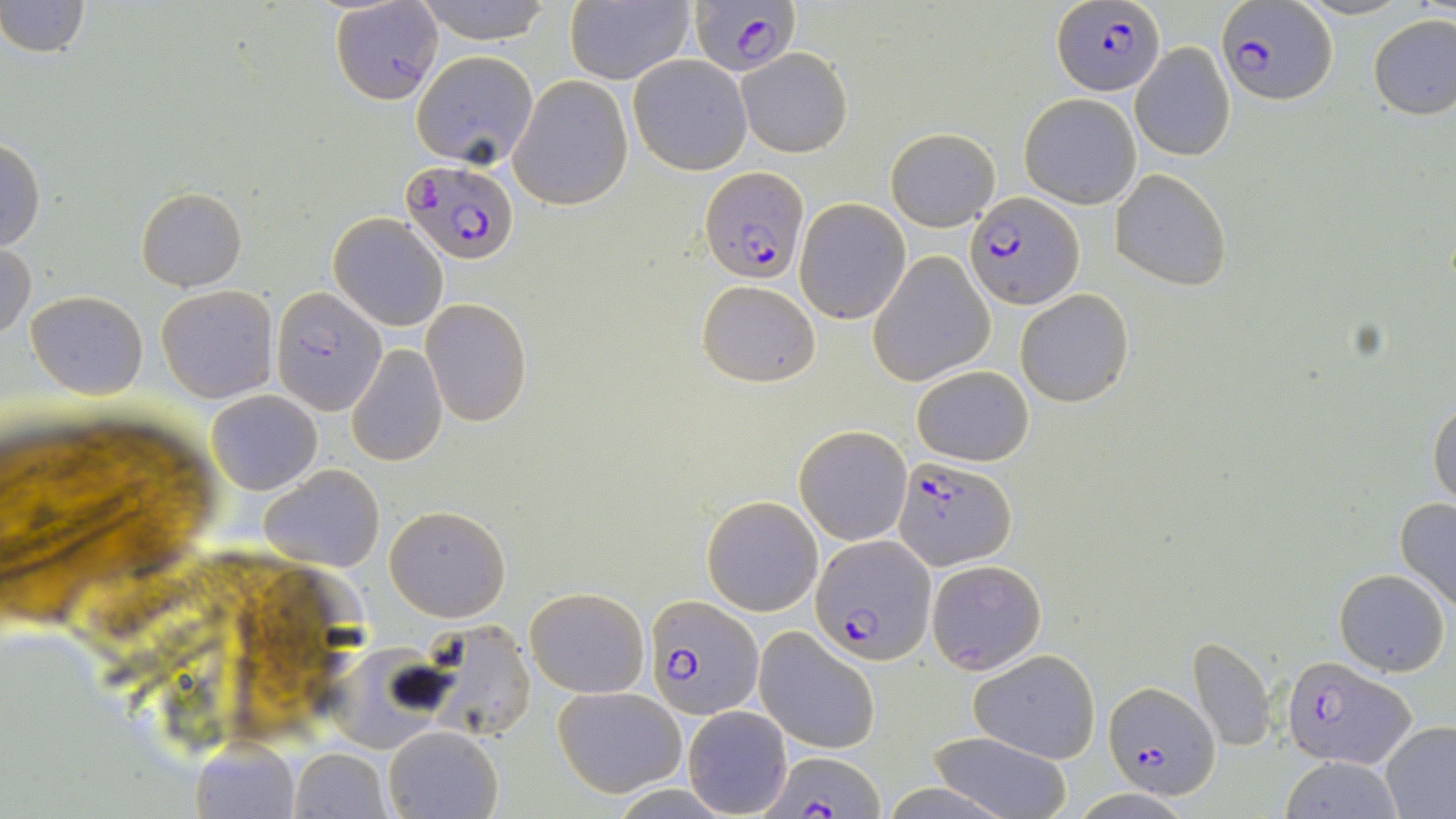 Approximate bounding boxes as named x1/y1/x2/y2 corners in pixels. Uninfected red blood cell locations: (x1=1, y1=0, x2=91, y2=58), (x1=410, y1=0, x2=559, y2=44), (x1=330, y1=1, x2=446, y2=103), (x1=564, y1=3, x2=695, y2=85), (x1=1366, y1=15, x2=1456, y2=120), (x1=1131, y1=43, x2=1235, y2=161), (x1=737, y1=49, x2=852, y2=158), (x1=411, y1=50, x2=539, y2=170), (x1=629, y1=55, x2=753, y2=174), (x1=510, y1=74, x2=635, y2=209), (x1=1019, y1=93, x2=1142, y2=208), (x1=885, y1=127, x2=1000, y2=231), (x1=0, y1=139, x2=46, y2=253), (x1=1110, y1=169, x2=1232, y2=290), (x1=137, y1=186, x2=247, y2=291), (x1=794, y1=199, x2=911, y2=323), (x1=330, y1=213, x2=448, y2=330), (x1=1, y1=240, x2=36, y2=339), (x1=870, y1=252, x2=994, y2=386), (x1=698, y1=278, x2=820, y2=386), (x1=155, y1=284, x2=278, y2=404), (x1=25, y1=288, x2=148, y2=399), (x1=272, y1=288, x2=388, y2=413), (x1=1015, y1=288, x2=1135, y2=408), (x1=422, y1=297, x2=531, y2=426), (x1=345, y1=343, x2=448, y2=468), (x1=910, y1=364, x2=1035, y2=467), (x1=207, y1=390, x2=322, y2=495), (x1=1427, y1=398, x2=1456, y2=511), (x1=795, y1=425, x2=912, y2=545), (x1=258, y1=464, x2=386, y2=572), (x1=703, y1=493, x2=823, y2=615), (x1=1394, y1=498, x2=1456, y2=612), (x1=383, y1=503, x2=511, y2=622), (x1=927, y1=559, x2=1048, y2=672), (x1=1334, y1=568, x2=1449, y2=676), (x1=525, y1=587, x2=648, y2=698), (x1=416, y1=618, x2=538, y2=739), (x1=754, y1=626, x2=881, y2=753), (x1=1188, y1=636, x2=1277, y2=751), (x1=315, y1=643, x2=438, y2=751), (x1=968, y1=649, x2=1101, y2=763), (x1=553, y1=687, x2=684, y2=797), (x1=681, y1=705, x2=792, y2=817), (x1=1380, y1=722, x2=1456, y2=816), (x1=383, y1=724, x2=504, y2=818), (x1=926, y1=731, x2=1073, y2=818), (x1=190, y1=738, x2=300, y2=818), (x1=287, y1=747, x2=392, y2=818), (x1=1277, y1=757, x2=1406, y2=817). Plasmodium falciparum-infected red blood cell locations: (x1=688, y1=1, x2=800, y2=79), (x1=1217, y1=1, x2=1335, y2=106), (x1=1052, y1=2, x2=1163, y2=95), (x1=399, y1=159, x2=519, y2=265), (x1=699, y1=166, x2=807, y2=284), (x1=967, y1=191, x2=1082, y2=309), (x1=894, y1=456, x2=1016, y2=571), (x1=812, y1=535, x2=935, y2=662), (x1=647, y1=595, x2=762, y2=717), (x1=1281, y1=654, x2=1414, y2=770), (x1=1103, y1=681, x2=1220, y2=800), (x1=763, y1=751, x2=884, y2=816). Slide-level diagnosis: Plasmodium falciparum. 1000x magnification. Light microscopy. May-Grünwald-Giemsa stain. One field of a larger specimen. Image is 1456×819 pixels. Thin blood smear.